State the blood parasite species.
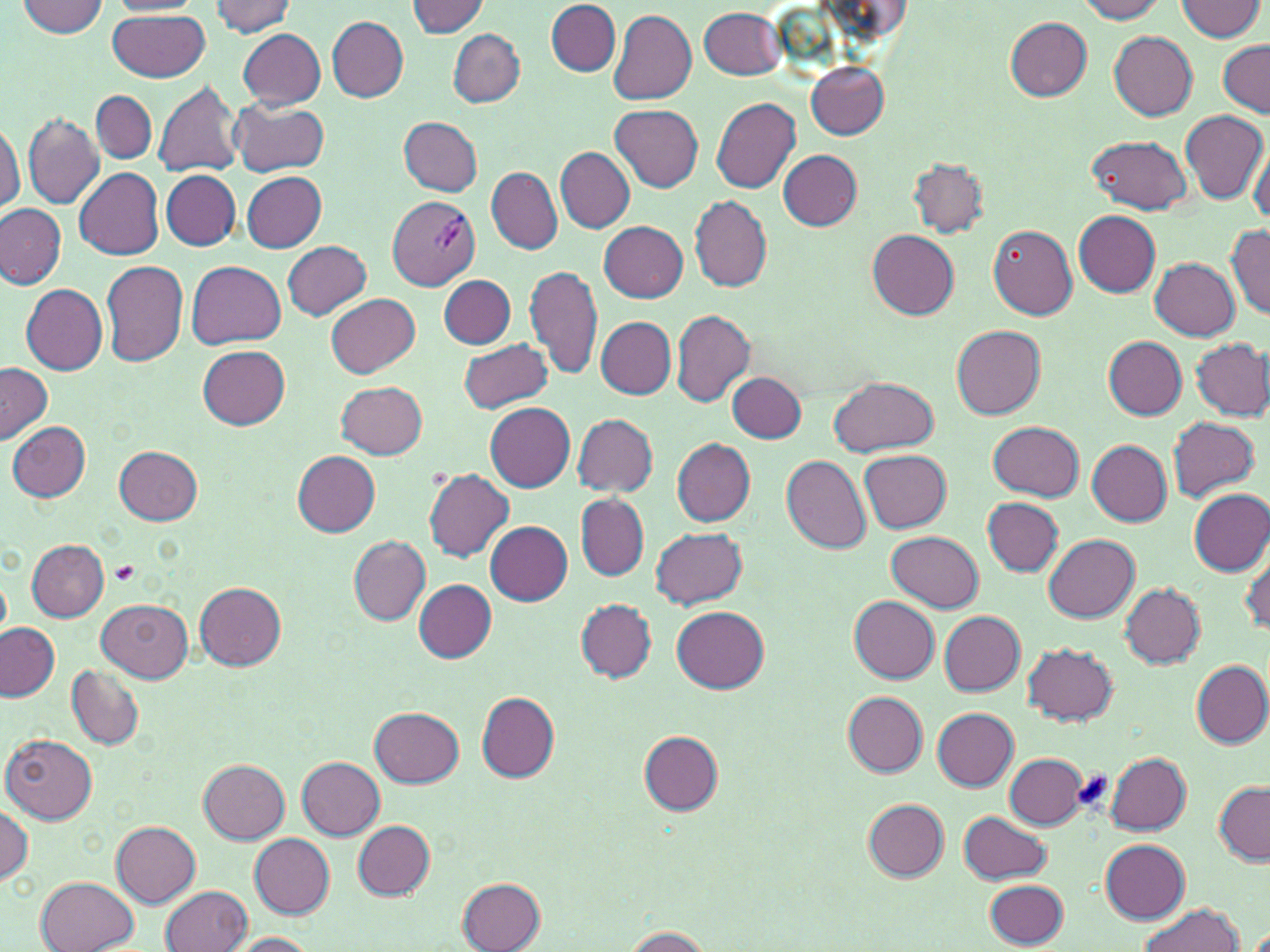

Plasmodium vivax.

Approximate bounding boxes as named x1/y1/x2/y2 corners in pixels. Uninfected red blood cell locations: (x1=1076, y1=0, x2=1168, y2=22), (x1=1176, y1=0, x2=1264, y2=41), (x1=17, y1=1, x2=107, y2=36), (x1=107, y1=1, x2=202, y2=15), (x1=209, y1=1, x2=296, y2=35), (x1=407, y1=1, x2=489, y2=37), (x1=547, y1=1, x2=620, y2=75), (x1=698, y1=7, x2=784, y2=80), (x1=608, y1=9, x2=697, y2=104), (x1=108, y1=10, x2=211, y2=82), (x1=328, y1=16, x2=409, y2=101), (x1=1004, y1=18, x2=1093, y2=100), (x1=238, y1=29, x2=325, y2=109), (x1=449, y1=29, x2=524, y2=107), (x1=1108, y1=31, x2=1198, y2=120), (x1=1217, y1=41, x2=1270, y2=117), (x1=805, y1=61, x2=890, y2=139), (x1=154, y1=78, x2=244, y2=180), (x1=91, y1=91, x2=156, y2=163), (x1=712, y1=96, x2=801, y2=193), (x1=230, y1=99, x2=329, y2=177), (x1=611, y1=105, x2=703, y2=192), (x1=1180, y1=111, x2=1267, y2=206), (x1=19, y1=115, x2=104, y2=210), (x1=400, y1=117, x2=483, y2=195), (x1=0, y1=121, x2=24, y2=214), (x1=1089, y1=135, x2=1193, y2=214), (x1=1249, y1=138, x2=1270, y2=226), (x1=555, y1=147, x2=634, y2=232), (x1=779, y1=150, x2=862, y2=228), (x1=909, y1=158, x2=988, y2=238), (x1=486, y1=166, x2=562, y2=255), (x1=75, y1=169, x2=164, y2=260), (x1=162, y1=170, x2=241, y2=250), (x1=241, y1=171, x2=327, y2=251), (x1=691, y1=195, x2=772, y2=291), (x1=0, y1=202, x2=67, y2=289), (x1=1074, y1=211, x2=1161, y2=295), (x1=599, y1=221, x2=688, y2=302), (x1=989, y1=225, x2=1078, y2=320), (x1=1227, y1=228, x2=1270, y2=319), (x1=868, y1=230, x2=960, y2=319), (x1=282, y1=241, x2=372, y2=320), (x1=1149, y1=256, x2=1240, y2=340), (x1=101, y1=260, x2=189, y2=366), (x1=187, y1=261, x2=286, y2=349), (x1=525, y1=265, x2=603, y2=381), (x1=440, y1=274, x2=515, y2=349), (x1=446, y1=275, x2=525, y2=412), (x1=22, y1=284, x2=108, y2=374), (x1=326, y1=294, x2=420, y2=377), (x1=670, y1=309, x2=754, y2=405), (x1=597, y1=317, x2=676, y2=398), (x1=950, y1=324, x2=1046, y2=419), (x1=1104, y1=337, x2=1188, y2=418), (x1=1182, y1=337, x2=1267, y2=503), (x1=459, y1=338, x2=551, y2=413), (x1=1192, y1=339, x2=1270, y2=420), (x1=199, y1=345, x2=289, y2=429), (x1=0, y1=362, x2=54, y2=443), (x1=727, y1=371, x2=807, y2=442), (x1=826, y1=378, x2=939, y2=456), (x1=335, y1=381, x2=427, y2=459), (x1=485, y1=403, x2=575, y2=492), (x1=572, y1=414, x2=659, y2=496), (x1=1167, y1=416, x2=1260, y2=502), (x1=989, y1=421, x2=1085, y2=500), (x1=8, y1=422, x2=90, y2=502), (x1=671, y1=437, x2=756, y2=525), (x1=1088, y1=440, x2=1172, y2=526), (x1=114, y1=446, x2=203, y2=525), (x1=292, y1=450, x2=381, y2=534), (x1=859, y1=450, x2=951, y2=533), (x1=782, y1=455, x2=872, y2=552), (x1=424, y1=468, x2=515, y2=562), (x1=1189, y1=489, x2=1270, y2=573), (x1=444, y1=495, x2=565, y2=596), (x1=576, y1=495, x2=647, y2=579), (x1=983, y1=498, x2=1063, y2=575), (x1=486, y1=521, x2=573, y2=606), (x1=650, y1=526, x2=747, y2=609), (x1=887, y1=530, x2=984, y2=611), (x1=1044, y1=533, x2=1140, y2=621), (x1=348, y1=535, x2=431, y2=625), (x1=26, y1=538, x2=110, y2=622), (x1=1241, y1=549, x2=1270, y2=637), (x1=414, y1=580, x2=497, y2=662), (x1=195, y1=581, x2=286, y2=670), (x1=1120, y1=582, x2=1206, y2=667), (x1=849, y1=595, x2=940, y2=683), (x1=98, y1=599, x2=192, y2=682), (x1=575, y1=599, x2=658, y2=682), (x1=672, y1=605, x2=770, y2=692), (x1=938, y1=610, x2=1025, y2=695), (x1=0, y1=623, x2=59, y2=701), (x1=1024, y1=643, x2=1118, y2=724), (x1=1191, y1=660, x2=1270, y2=747), (x1=66, y1=663, x2=145, y2=748), (x1=476, y1=692, x2=559, y2=782), (x1=844, y1=693, x2=927, y2=776), (x1=370, y1=707, x2=464, y2=788), (x1=933, y1=708, x2=1017, y2=791), (x1=638, y1=731, x2=723, y2=815), (x1=2, y1=734, x2=97, y2=823), (x1=1105, y1=752, x2=1191, y2=834), (x1=1005, y1=753, x2=1088, y2=828), (x1=297, y1=757, x2=385, y2=840), (x1=200, y1=760, x2=287, y2=843), (x1=1213, y1=781, x2=1270, y2=864), (x1=863, y1=799, x2=948, y2=880), (x1=0, y1=800, x2=32, y2=885), (x1=959, y1=811, x2=1052, y2=884), (x1=110, y1=820, x2=201, y2=906), (x1=352, y1=821, x2=433, y2=900), (x1=250, y1=834, x2=335, y2=918), (x1=1100, y1=839, x2=1190, y2=923), (x1=36, y1=875, x2=140, y2=952), (x1=457, y1=878, x2=547, y2=951), (x1=985, y1=878, x2=1068, y2=949), (x1=162, y1=884, x2=252, y2=951), (x1=1136, y1=903, x2=1243, y2=952), (x1=615, y1=926, x2=718, y2=951), (x1=224, y1=932, x2=319, y2=952). Platelet locations: (x1=111, y1=562, x2=140, y2=584), (x1=1069, y1=769, x2=1114, y2=815). Plasmodium vivax-infected red blood cell locations: (x1=388, y1=195, x2=480, y2=290). May-Grünwald-Giemsa-stained preparation. Optical microscopy. Image is 1270×952 pixels. Thin blood smear. Captured at 1000x magnification. One field of a larger specimen.